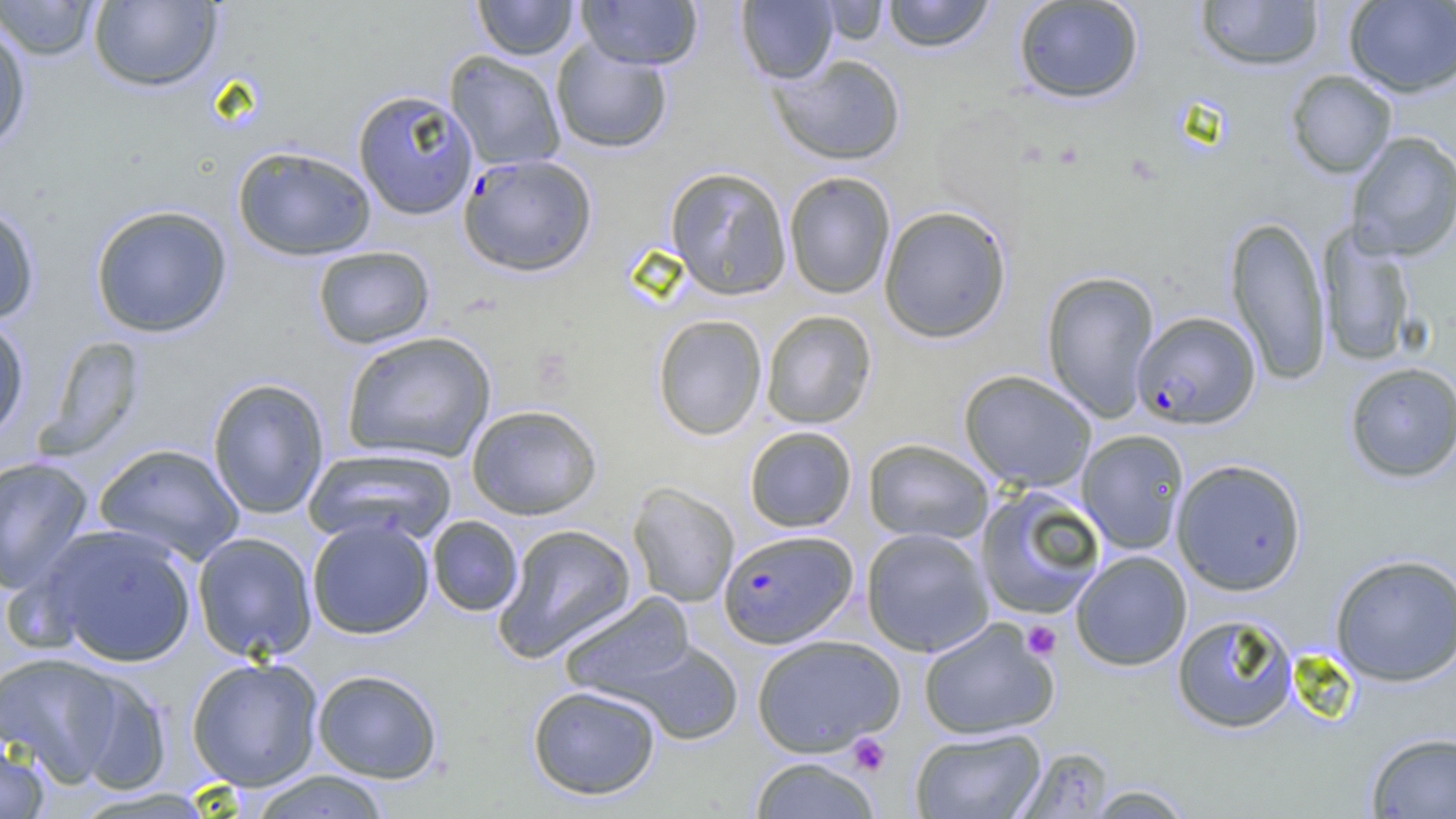
Summary:
  - Coordinate format: approximate bounding boxes as (x1, y1, x2, y2) in pixels
  - Platelet locations: (1021, 621, 1062, 660), (848, 733, 891, 776)
  - Uninfected red blood cell locations: (473, 0, 579, 60), (576, 0, 702, 69), (736, 0, 838, 84), (881, 0, 997, 52), (1012, 0, 1145, 104), (1194, 0, 1325, 72), (1, 1, 102, 61), (88, 1, 223, 92), (817, 1, 890, 45), (1344, 1, 1456, 97), (0, 16, 32, 155), (550, 39, 673, 154), (444, 51, 567, 171), (770, 53, 907, 166), (1285, 70, 1397, 179), (352, 89, 479, 220), (1345, 131, 1456, 260), (232, 145, 376, 261), (664, 166, 792, 300), (783, 171, 896, 299), (0, 200, 41, 325), (89, 204, 233, 338), (878, 205, 1013, 343), (1225, 215, 1332, 386), (1317, 224, 1417, 368), (312, 246, 435, 349), (1041, 270, 1160, 421), (760, 310, 876, 429), (652, 314, 767, 440), (0, 315, 31, 444), (340, 331, 497, 463), (40, 337, 146, 459), (1344, 362, 1456, 483), (958, 369, 1097, 492), (207, 378, 330, 519), (466, 404, 603, 520), (743, 425, 857, 532), (1077, 429, 1190, 554), (863, 438, 994, 544), (93, 442, 245, 564), (304, 447, 457, 546), (0, 455, 94, 595), (1171, 458, 1307, 596), (627, 481, 740, 608), (973, 485, 1107, 619), (426, 515, 523, 616), (306, 517, 436, 639), (41, 523, 198, 667), (492, 523, 637, 662), (860, 527, 994, 657), (192, 532, 318, 662), (1070, 550, 1192, 671), (1329, 553, 1456, 687), (559, 592, 697, 700), (1171, 613, 1299, 734), (918, 617, 1060, 740), (750, 634, 905, 756), (623, 640, 743, 745), (0, 651, 129, 786), (185, 656, 324, 791), (311, 669, 443, 783), (65, 670, 172, 795), (527, 685, 662, 800), (909, 727, 1047, 819), (1364, 731, 1456, 818), (0, 737, 50, 818), (1013, 746, 1116, 818), (747, 756, 883, 818), (245, 770, 393, 819), (1082, 784, 1197, 818)
  - Plasmodium falciparum-infected red blood cell locations: (458, 153, 597, 277), (1132, 311, 1260, 429), (719, 529, 857, 648)
  - Slide-level diagnosis: Plasmodium falciparum
  - Modality: optical microscopy
  - Preparation: thin blood film
  - Field of view: single
  - Magnification: 1000x
  - Image size: 1456×819 pixels